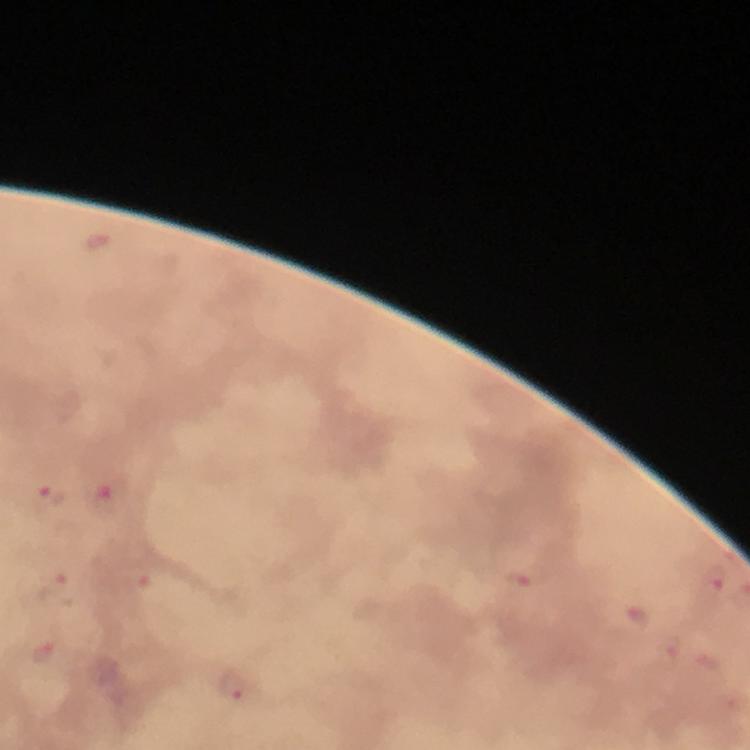
Plasmodium parasite locations = approximate centers as (x, y) in pixels: (98, 240), (49, 496), (107, 498), (714, 578), (522, 580), (54, 587), (637, 617), (671, 649), (42, 652), (234, 687)
immersion oil = used
image size = 750×750 pixels
preparation = thick smear
context = from a diagnostic examination for malaria
stain = Giemsa
magnification = 100x
capture = smartphone mounted on the microscope
cropped from = a single field of view